Name the parasite shown.
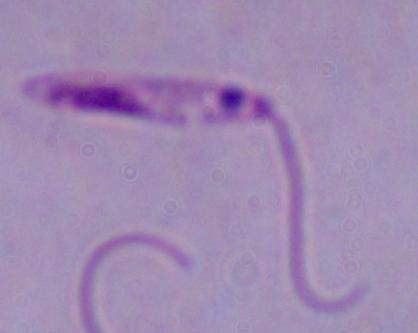
This is Leishmania.

1000x magnification. Micrograph.